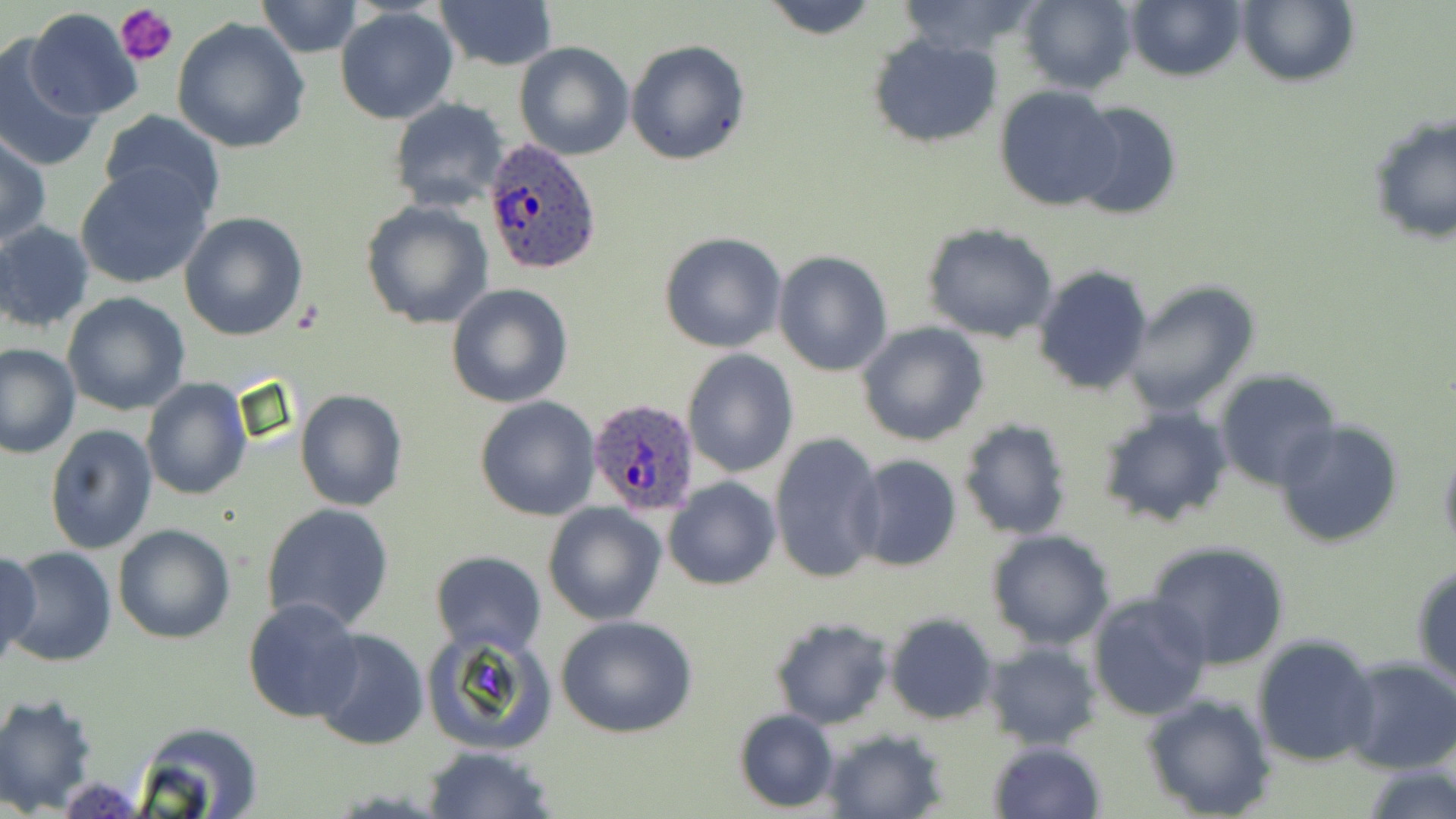
Plasmodium ovale-infected red blood cell locations = approximate bounding boxes as (x1, y1, x2, y2) in pixels: (482, 137, 603, 276), (585, 399, 702, 518)
slide-level diagnosis = Plasmodium ovale
modality = light microscopy
platelet locations = approximate bounding boxes as (x1, y1, x2, y2) in pixels: (116, 3, 178, 67)
uninfected red blood cell locations = approximate bounding boxes as (x1, y1, x2, y2) in pixels: (255, 0, 363, 57), (757, 0, 881, 39), (894, 0, 1046, 60), (1017, 0, 1137, 93), (1127, 0, 1247, 81), (1238, 0, 1358, 87), (434, 1, 558, 72), (334, 7, 459, 125), (24, 9, 142, 122), (173, 18, 311, 155), (867, 35, 1001, 148), (626, 39, 749, 164), (0, 41, 98, 173), (514, 41, 635, 161), (994, 85, 1126, 211), (387, 98, 510, 211), (1068, 101, 1183, 220), (99, 111, 224, 217), (1366, 114, 1456, 246), (0, 132, 51, 250), (75, 165, 210, 289), (360, 199, 493, 331), (179, 212, 309, 341), (0, 221, 96, 333), (921, 223, 1061, 344), (657, 231, 787, 353), (772, 250, 892, 377), (1032, 264, 1154, 396), (1122, 279, 1259, 415), (446, 283, 573, 408), (62, 291, 190, 416), (856, 321, 989, 446), (0, 344, 80, 459), (681, 349, 800, 478), (1215, 370, 1341, 491), (142, 377, 251, 500), (295, 390, 407, 510), (474, 396, 599, 521), (1095, 405, 1233, 529), (957, 416, 1073, 540), (1273, 419, 1404, 549), (45, 425, 157, 554), (770, 433, 887, 586), (1437, 442, 1456, 559), (848, 454, 962, 574), (664, 477, 781, 589), (543, 501, 668, 624), (260, 502, 395, 632), (112, 523, 236, 644), (985, 529, 1115, 650), (1146, 539, 1291, 670), (3, 547, 118, 666), (0, 549, 42, 666), (429, 551, 547, 658), (1410, 560, 1456, 689), (1087, 591, 1214, 722), (242, 596, 365, 723), (885, 613, 998, 724), (554, 614, 698, 739), (769, 616, 893, 729), (884, 624, 1102, 736), (311, 628, 429, 751), (424, 630, 557, 756), (1251, 633, 1381, 766), (981, 640, 1101, 750), (1339, 657, 1456, 773), (1139, 691, 1279, 819), (0, 693, 100, 813), (733, 709, 839, 812), (130, 723, 266, 818), (822, 727, 949, 818), (987, 740, 1105, 819), (424, 744, 556, 819), (1362, 763, 1454, 819)
preparation = thin blood film
magnification = 1000x
image size = 1456×819 pixels
stain = May-Grünwald-Giemsa
field of view = single